Outline each uninfected red blood cell.
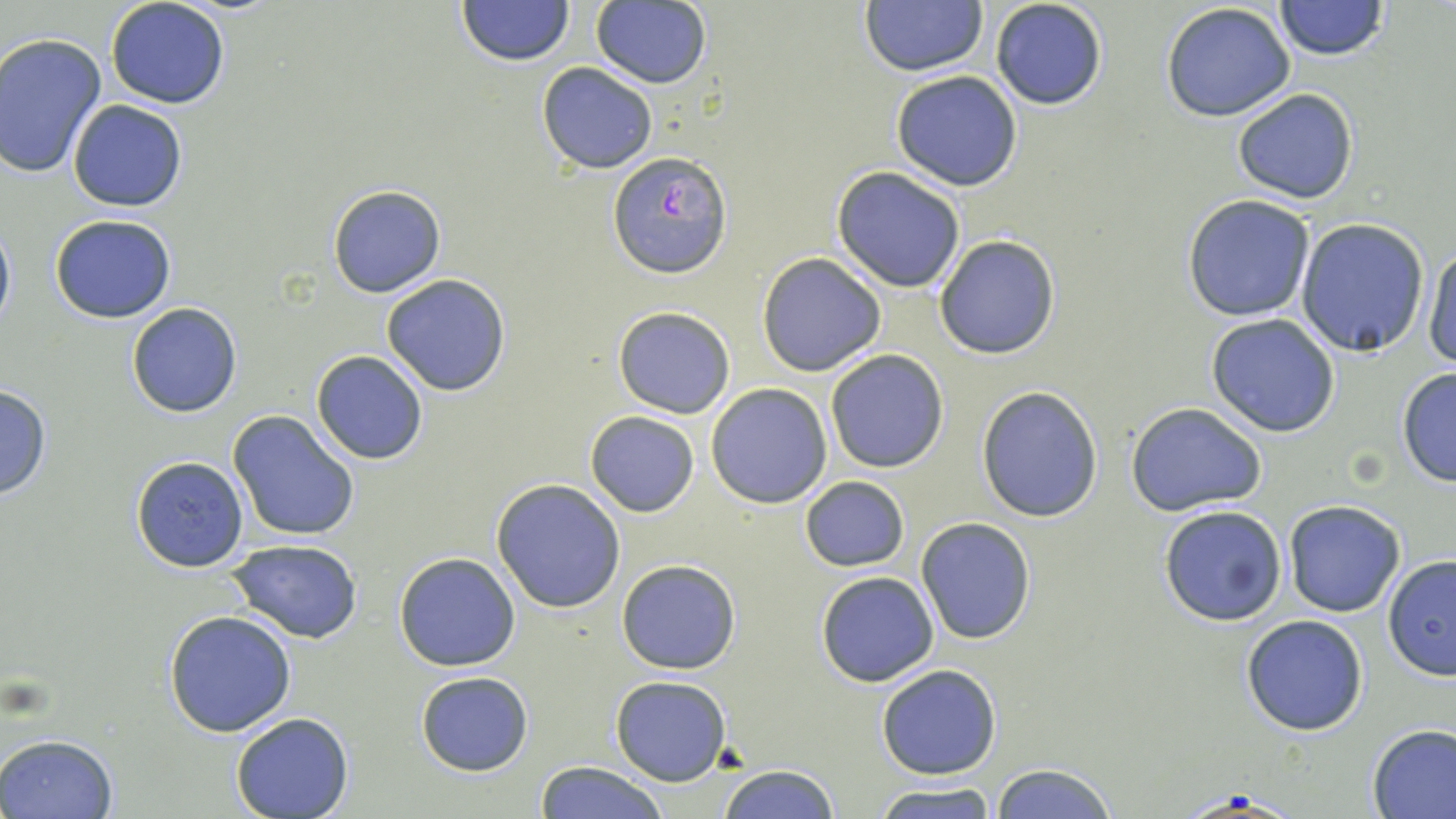
Approximate bounding boxes as (x1, y1, x2, y2) in pixels.
Uninfected red blood cells: (105, 0, 231, 108), (456, 0, 574, 67), (990, 0, 1109, 112), (1274, 0, 1389, 59), (591, 1, 711, 89), (860, 2, 988, 77), (1160, 3, 1297, 121), (0, 32, 106, 182), (536, 62, 658, 173), (891, 69, 1023, 191), (1231, 88, 1360, 204), (67, 99, 187, 211), (832, 166, 966, 292), (327, 184, 446, 298), (1182, 193, 1316, 322), (48, 214, 179, 324), (0, 216, 14, 338), (1297, 218, 1430, 357), (934, 237, 1059, 359), (1423, 240, 1456, 371), (757, 252, 886, 377), (380, 273, 512, 395), (127, 303, 242, 418), (612, 307, 737, 419), (1206, 314, 1342, 438), (826, 348, 949, 473), (311, 351, 430, 465), (1396, 366, 1456, 487), (0, 383, 52, 499), (706, 383, 833, 509), (976, 385, 1105, 523), (1126, 403, 1267, 516), (228, 410, 360, 542), (585, 411, 699, 518), (130, 455, 249, 573), (800, 476, 908, 572), (491, 478, 626, 613), (1283, 499, 1406, 617), (1158, 505, 1287, 627), (916, 517, 1035, 645), (226, 538, 363, 644), (394, 552, 521, 672), (1382, 556, 1456, 682), (616, 560, 741, 675), (814, 569, 939, 687), (163, 609, 297, 737), (1241, 614, 1369, 736), (876, 664, 1002, 780), (416, 671, 534, 776), (610, 676, 730, 785), (229, 713, 355, 819), (1367, 723, 1456, 819), (2, 733, 118, 817), (533, 761, 669, 819), (989, 763, 1120, 818), (716, 764, 839, 819), (872, 783, 998, 818).

slide_level_diagnosis: Plasmodium falciparum
preparation: thin blood smear
image_size: 1456×819 pixels
modality: optical microscopy
stain: May-Grünwald-Giemsa
field_of_view: single
magnification: 1000x
plasmodium_falciparum_infected_red_blood_cell_locations: 'approximate bounding boxes as (x1, y1, x2, y2) in pixels: (606, 152, 730, 279)'